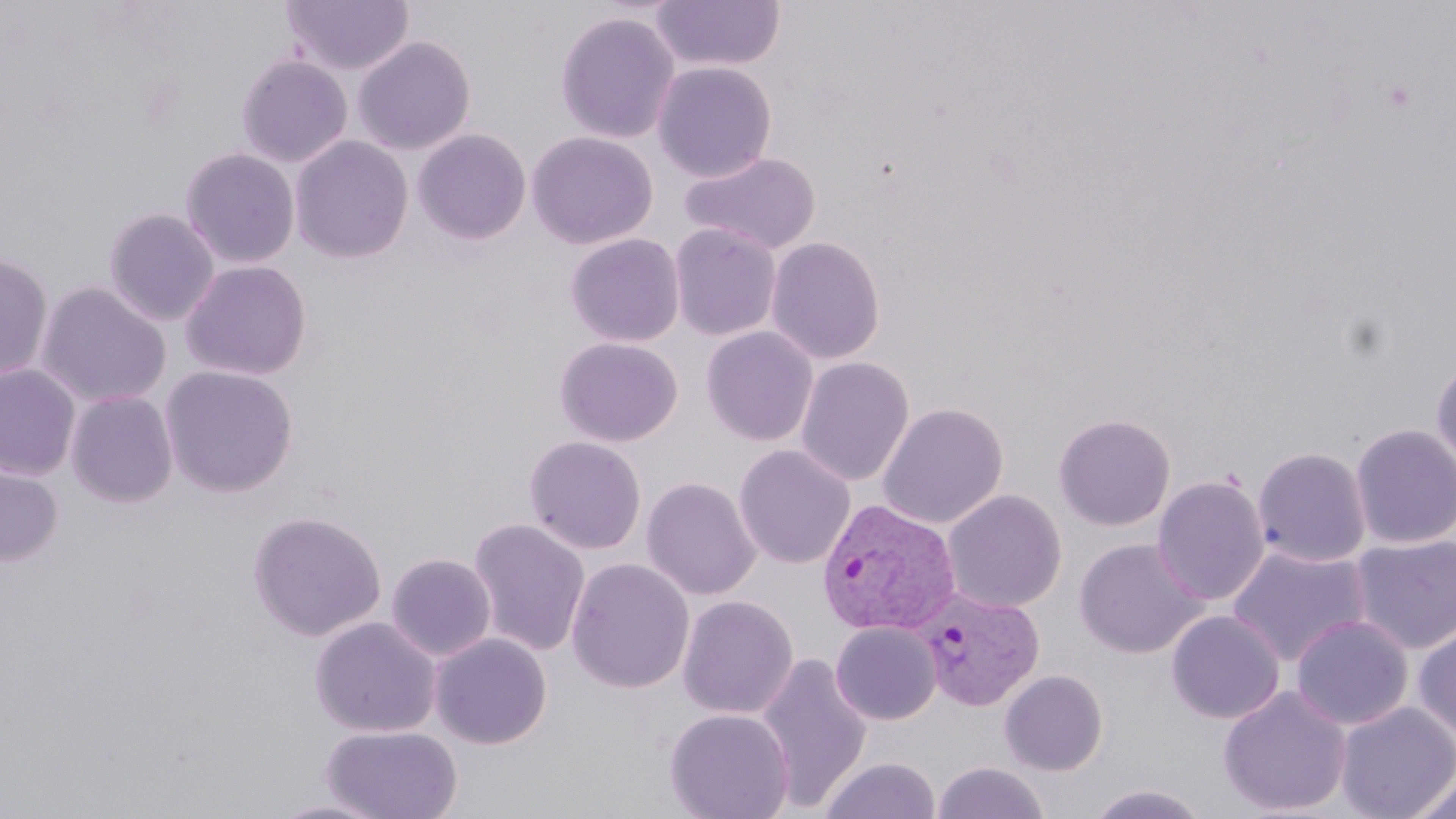
Approximate bounding boxes as named x1/y1/x2/y2 corners in pixels. Plasmodium vivax-infected red blood cell locations: (x1=816, y1=499, x2=962, y2=638), (x1=914, y1=588, x2=1041, y2=714). Uninfected red blood cell locations: (x1=281, y1=0, x2=415, y2=76), (x1=649, y1=1, x2=785, y2=73), (x1=555, y1=11, x2=681, y2=144), (x1=352, y1=36, x2=476, y2=155), (x1=236, y1=54, x2=353, y2=168), (x1=652, y1=61, x2=777, y2=181), (x1=412, y1=128, x2=532, y2=245), (x1=526, y1=131, x2=658, y2=250), (x1=288, y1=135, x2=414, y2=263), (x1=180, y1=147, x2=300, y2=268), (x1=680, y1=151, x2=821, y2=255), (x1=103, y1=207, x2=220, y2=326), (x1=669, y1=222, x2=782, y2=341), (x1=565, y1=233, x2=685, y2=347), (x1=765, y1=236, x2=885, y2=365), (x1=0, y1=253, x2=54, y2=383), (x1=179, y1=259, x2=313, y2=380), (x1=34, y1=281, x2=172, y2=409), (x1=700, y1=326, x2=819, y2=446), (x1=554, y1=337, x2=684, y2=447), (x1=1431, y1=355, x2=1456, y2=475), (x1=794, y1=356, x2=915, y2=487), (x1=0, y1=364, x2=81, y2=480), (x1=160, y1=365, x2=299, y2=498), (x1=65, y1=390, x2=178, y2=507), (x1=877, y1=402, x2=1009, y2=528), (x1=1053, y1=413, x2=1176, y2=531), (x1=1350, y1=423, x2=1456, y2=548), (x1=524, y1=436, x2=647, y2=554), (x1=733, y1=444, x2=856, y2=569), (x1=1252, y1=447, x2=1372, y2=568), (x1=0, y1=451, x2=64, y2=567), (x1=1152, y1=475, x2=1270, y2=606), (x1=641, y1=477, x2=761, y2=601), (x1=941, y1=489, x2=1066, y2=612), (x1=247, y1=509, x2=387, y2=642), (x1=467, y1=518, x2=592, y2=657), (x1=1350, y1=534, x2=1456, y2=654), (x1=1074, y1=537, x2=1208, y2=659), (x1=1227, y1=545, x2=1372, y2=668), (x1=386, y1=553, x2=496, y2=661), (x1=566, y1=558, x2=695, y2=693), (x1=677, y1=595, x2=798, y2=719), (x1=1166, y1=610, x2=1285, y2=725), (x1=1291, y1=615, x2=1414, y2=730), (x1=310, y1=616, x2=441, y2=737), (x1=1412, y1=621, x2=1456, y2=743), (x1=830, y1=622, x2=941, y2=725), (x1=429, y1=632, x2=552, y2=749), (x1=753, y1=653, x2=874, y2=812), (x1=999, y1=670, x2=1109, y2=775), (x1=1218, y1=685, x2=1352, y2=817), (x1=1335, y1=702, x2=1456, y2=819), (x1=664, y1=708, x2=795, y2=819), (x1=321, y1=724, x2=463, y2=819), (x1=818, y1=757, x2=940, y2=818), (x1=932, y1=761, x2=1050, y2=818), (x1=1408, y1=772, x2=1456, y2=819), (x1=1087, y1=784, x2=1211, y2=819), (x1=266, y1=797, x2=394, y2=818). Slide-level diagnosis: Plasmodium vivax. Image is 1456×819 pixels. Light microscopy. One field of a larger specimen. 1000x magnification. Thin blood smear. May-Grünwald-Giemsa-stained preparation.